Outline each blood parasite and name the species.
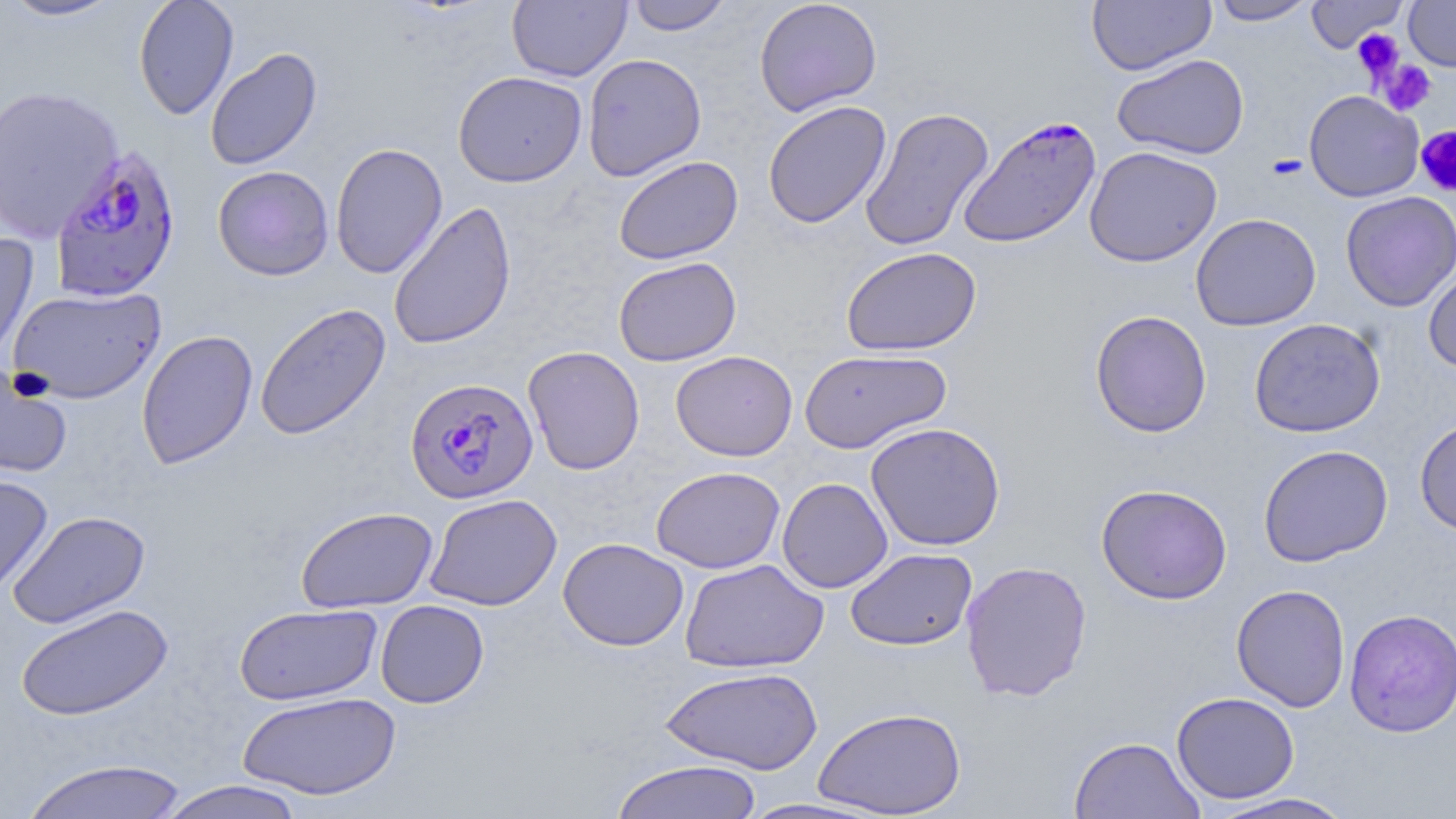
Approximate bounding boxes as (x1, y1, x2, y2) in pixels.
Plasmodium falciparum-infected red blood cells: (958, 114, 1102, 249), (50, 145, 183, 303), (404, 376, 538, 504).
No Plasmodium ovale, Plasmodium malariae, Plasmodium vivax, Babesia divergens, or Trypanosoma brucei observed.

Uninfected red blood cell locations: (2, 0, 123, 22), (133, 0, 239, 120), (625, 0, 734, 35), (753, 0, 882, 116), (1087, 0, 1216, 75), (1207, 0, 1318, 26), (1306, 0, 1408, 52), (1403, 0, 1456, 72), (507, 1, 632, 82), (205, 48, 323, 171), (582, 53, 707, 181), (1112, 53, 1249, 160), (452, 71, 587, 187), (0, 85, 124, 242), (1304, 90, 1424, 202), (762, 100, 892, 229), (860, 106, 994, 252), (330, 142, 448, 280), (1084, 145, 1222, 267), (613, 155, 743, 264), (212, 165, 334, 281), (1341, 191, 1456, 311), (388, 200, 516, 351), (1190, 213, 1321, 332), (0, 233, 40, 370), (840, 246, 982, 356), (613, 257, 741, 366), (1423, 264, 1456, 373), (7, 286, 166, 403), (255, 303, 392, 441), (1090, 310, 1212, 437), (1249, 317, 1385, 438), (136, 329, 258, 469), (523, 345, 645, 475), (799, 348, 952, 454), (670, 350, 798, 461), (0, 364, 73, 479), (1414, 417, 1456, 536), (865, 422, 1005, 551), (1258, 444, 1393, 567), (651, 466, 785, 573), (0, 473, 53, 596), (777, 477, 892, 593), (1095, 483, 1233, 605), (424, 493, 562, 611), (295, 506, 438, 613), (7, 510, 151, 630), (558, 537, 689, 651), (845, 548, 977, 651), (679, 558, 829, 673), (960, 559, 1093, 702), (1231, 584, 1351, 712), (375, 600, 489, 708), (15, 603, 173, 721), (234, 603, 382, 706), (1343, 608, 1456, 738), (659, 666, 823, 775), (237, 691, 401, 800), (1171, 691, 1299, 804), (813, 706, 966, 817), (1068, 736, 1205, 819), (18, 757, 193, 818), (610, 759, 764, 819), (154, 780, 310, 819), (1204, 792, 1358, 819), (732, 797, 886, 818). Platelet locations: (1353, 28, 1404, 80), (1378, 60, 1437, 116), (1415, 126, 1456, 198). Slide-level diagnosis: Plasmodium falciparum. One field of a larger specimen. Thin blood smear. Captured at 1000x magnification. Optical microscopy. May-Grünwald-Giemsa stain. Image is 1456×819 pixels.